State which parasite is depicted.
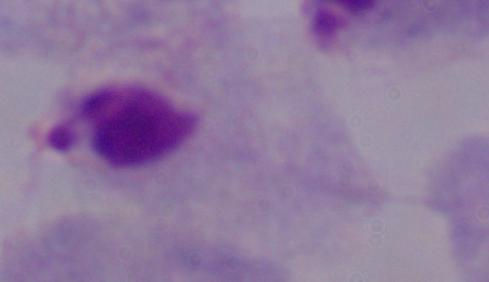

This is a trichomonad.

{
  "modality": "photomicrograph",
  "magnification": "1000x"
}